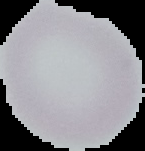

preparation = thin blood film
image size = 145×151 pixels
image type = segmented cell region with the area outside set to black
result = no Plasmodium parasites seen